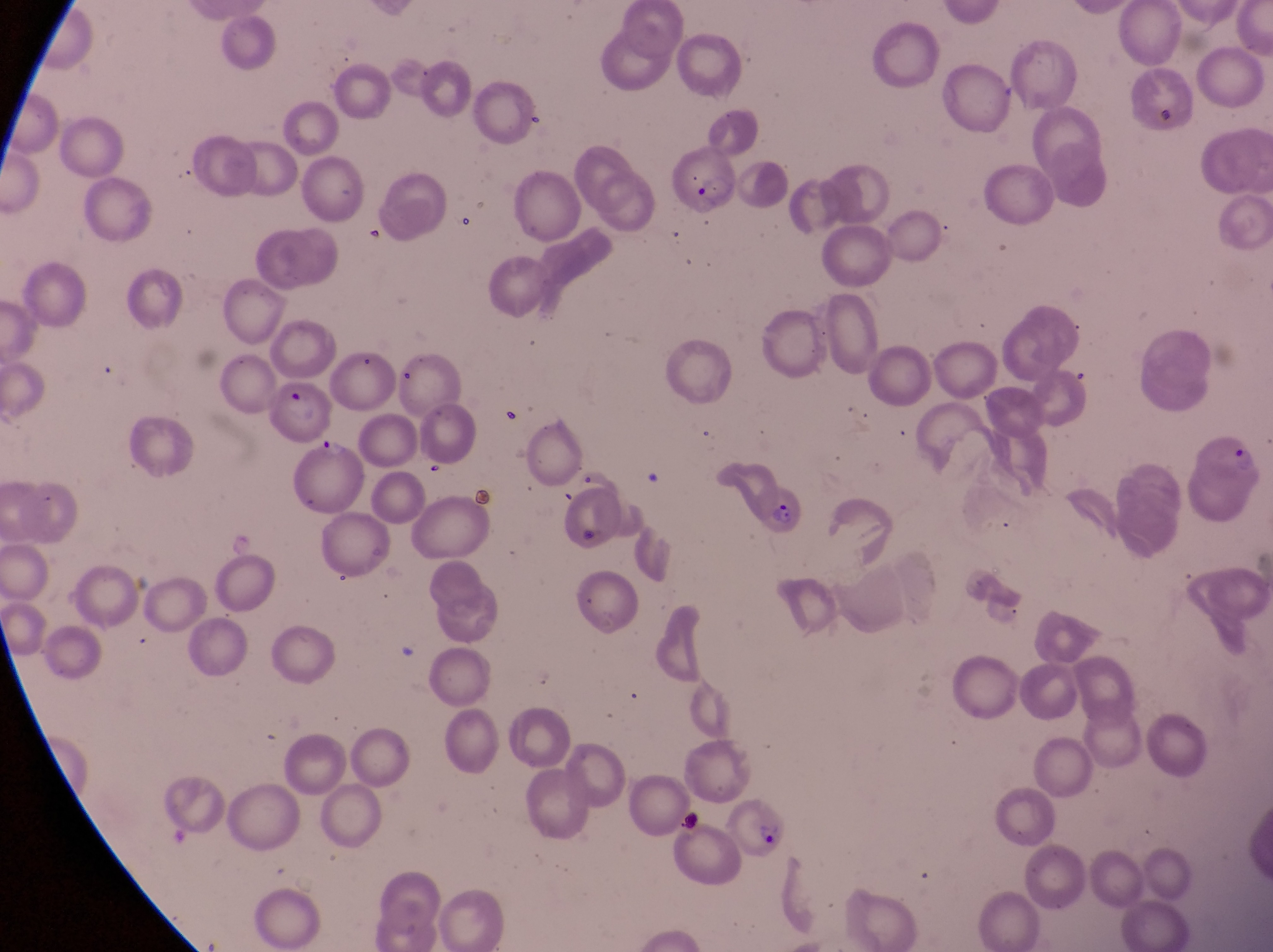
{
  "parasitised_red_blood_cell_locations": "approximate bounding boxes as [left, top, right, bottom] in pixels: [657, 145, 739, 225], [274, 379, 337, 446], [1199, 427, 1266, 502], [751, 479, 808, 536], [712, 794, 792, 862]",
  "country": "Uganda",
  "preparation": "thin blood smear",
  "capture": "smartphone photograph through the eyepiece of an Olympus CX-23 microscope",
  "trophozoite_locations": "approximate bounding boxes as [left, top, right, bottom] in pixels: [315, 429, 347, 462]",
  "field_of_view": "single",
  "image_size": "1273×952 pixels",
  "magnification": "1000x"
}